Identify the cell.
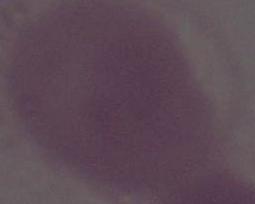
This is an erythrocyte.

magnification = 1000x
modality = micrograph